Give the preparation type.
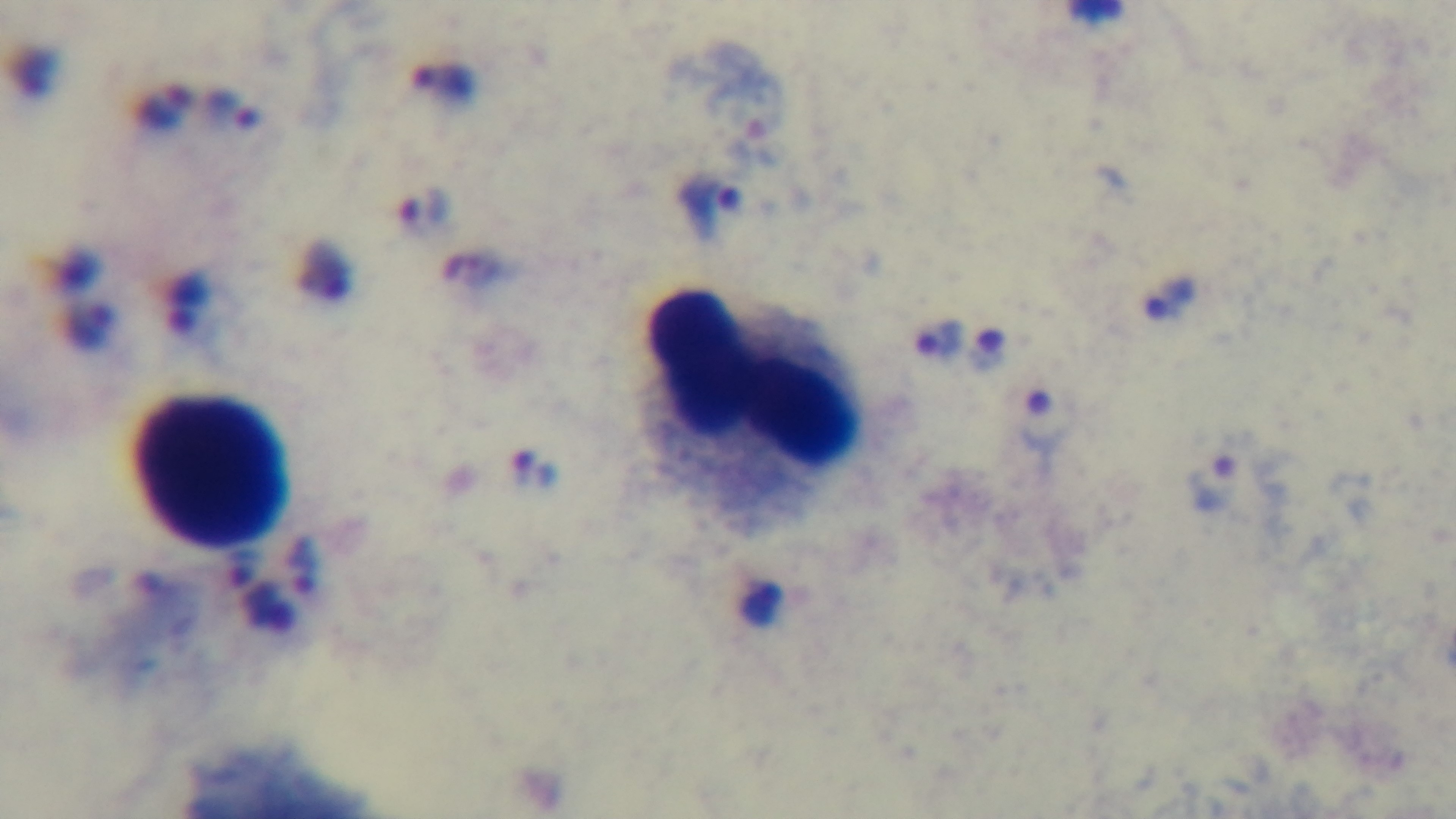
A thick smear.

Mounted 4K digital camera. Light microscopy. Giemsa stain. Single field of view. Malaria status: infected. Oil-immersion objective, 100x.